State which parasite is depicted.
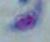

Toxoplasma gondii.

Summary:
  - Magnification: 1000x
  - Modality: photomicrograph